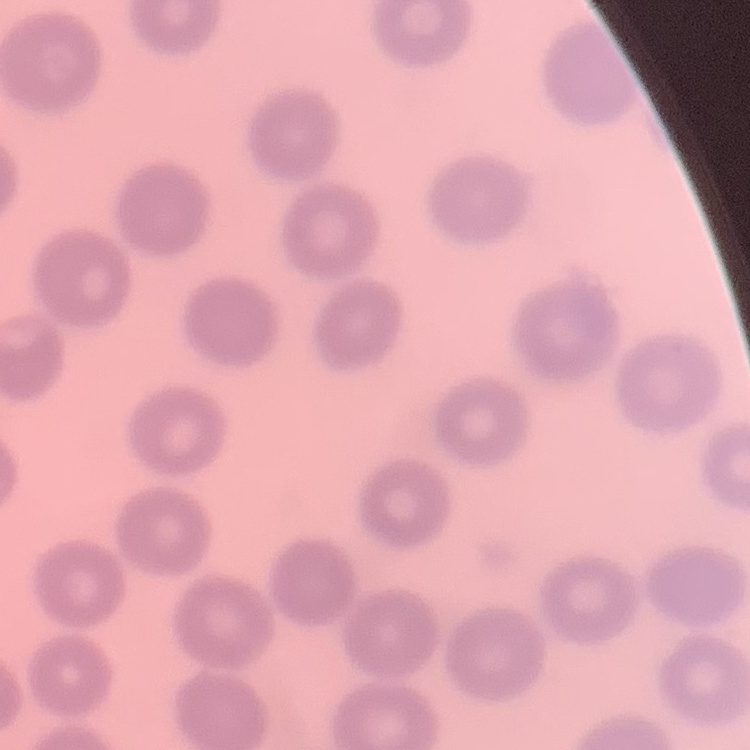
Summary:
  - Red blood cell morphology: no rouleaux formation
  - Stain: Field's or Giemsa
  - Preparation: thin peripheral smear
  - Image type: square crop of a larger photomicrograph